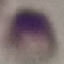

Result: negative for malaria parasites. Photographed with a smartphone camera at the microscope eyepiece. Thin blood film. Giemsa stain. Cell patch, automatically extracted from a larger field of view and resized to 64 × 64 pixels.